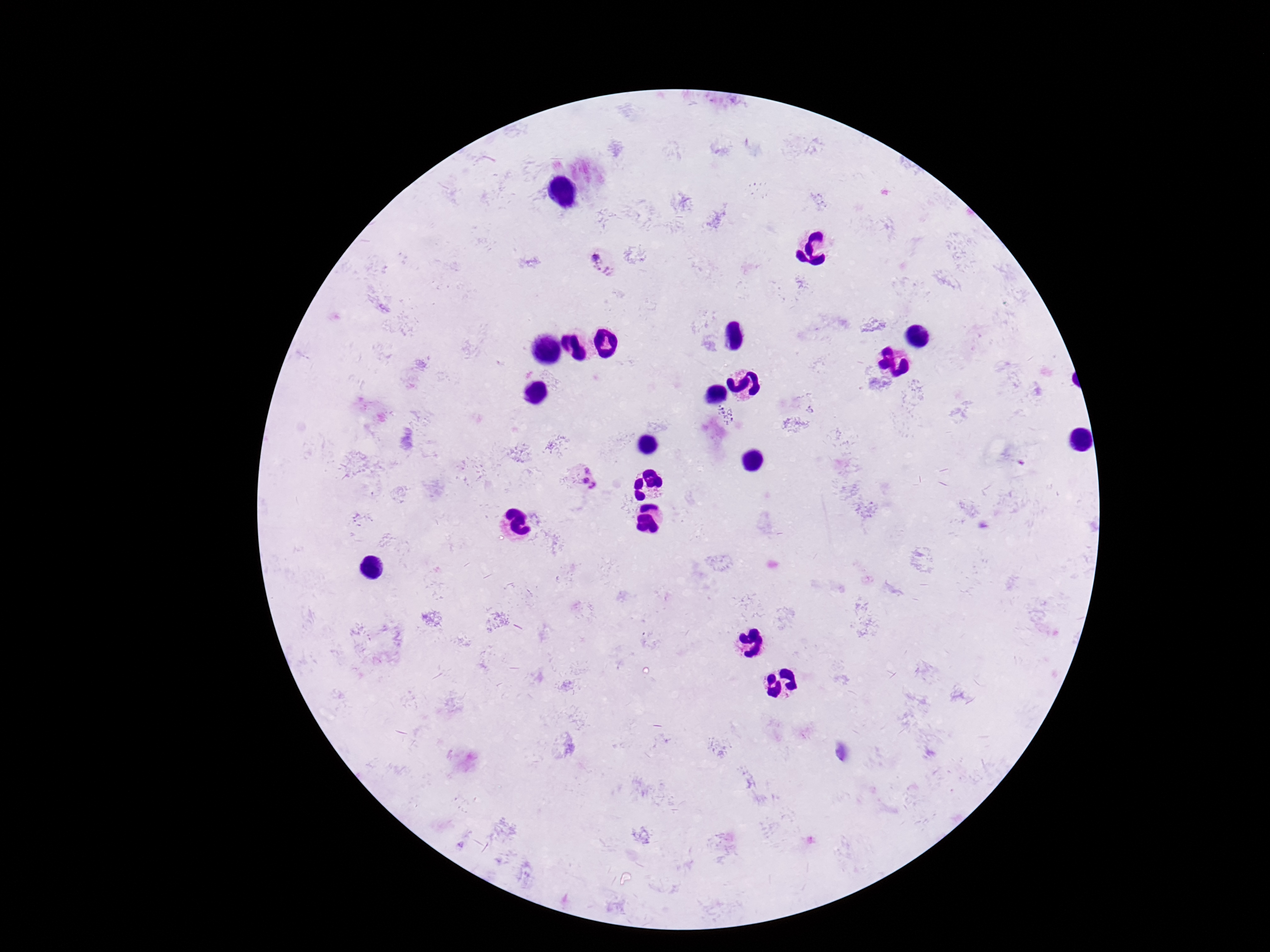

Approximate object centers, in pixels from the top-left corner. Plasmodium parasite locations: (x=602, y=263), (x=584, y=477). Image is 1270×952 pixels. Single field of view. Patient malaria status: positive. Thick blood smear. 100x magnification. Giemsa stain. Smartphone photograph taken through the microscope eyepiece.